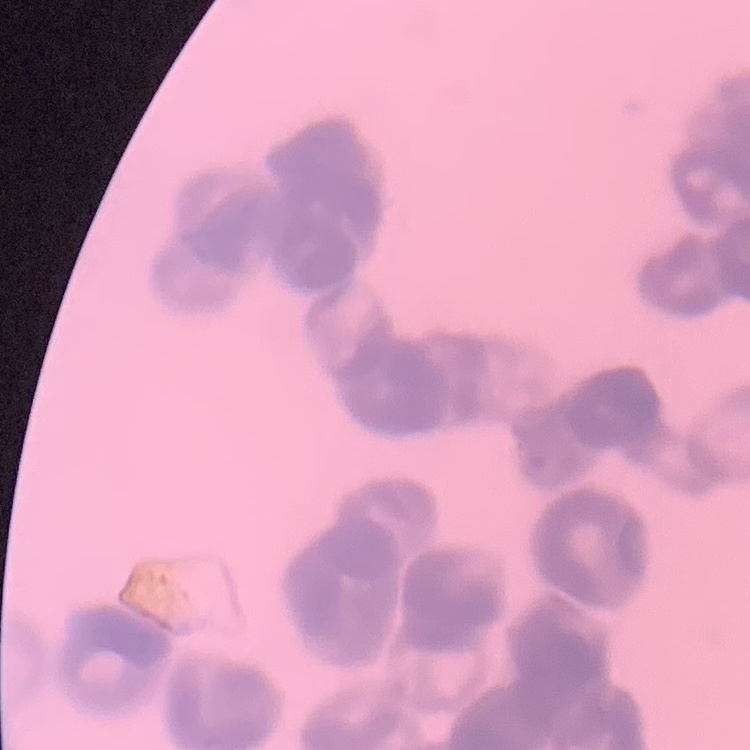

The erythrocytes exhibit rouleaux formation. Thin peripheral smear. Field's or Giemsa stain. Square crop of a larger photomicrograph.